Evaluate for Plasmodium parasites.
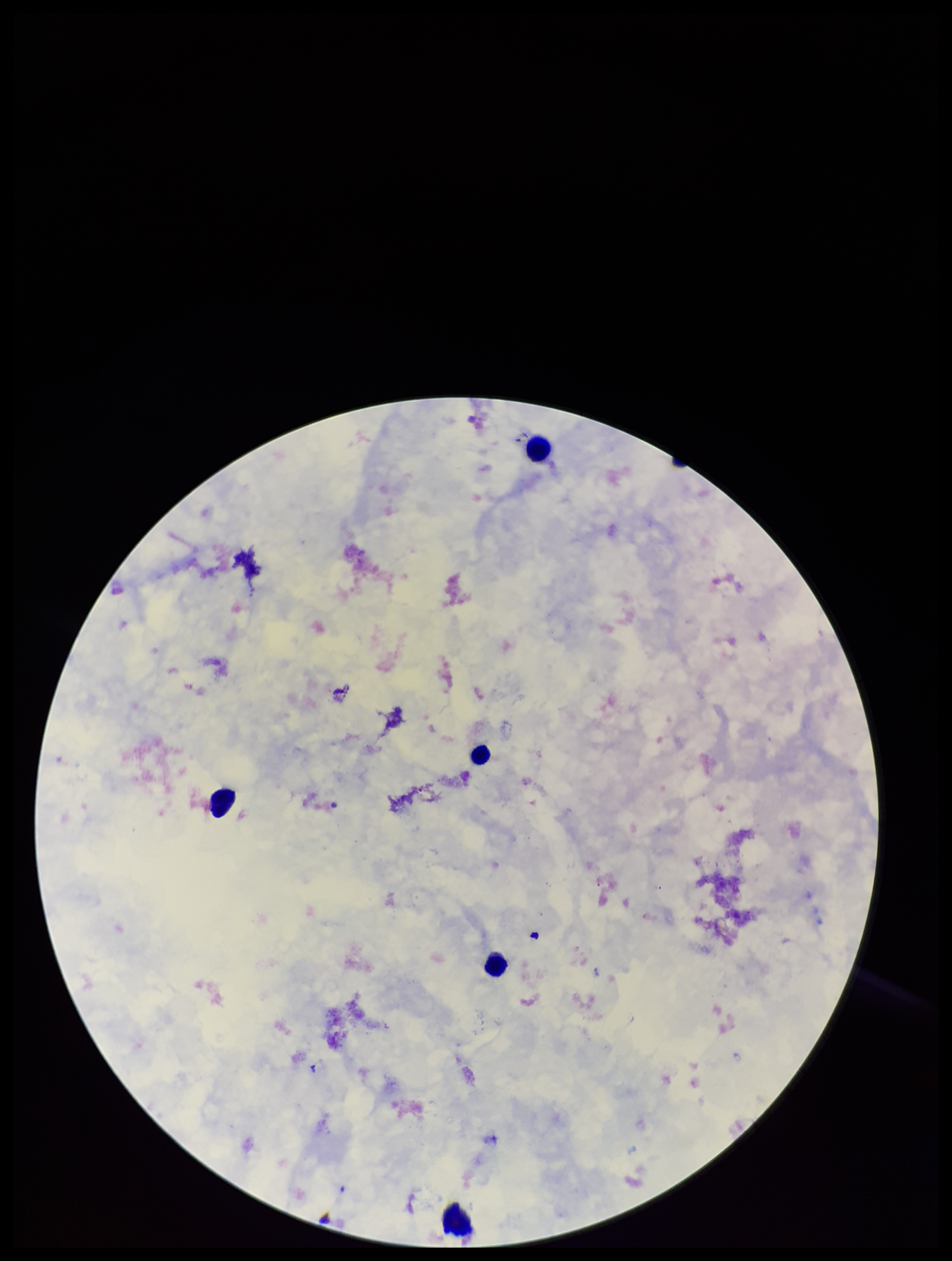

None detected.

Summary:
  - Leukocyte count: 5
  - Stain: Giemsa
  - Preparation: thick
  - Patient malaria status: negative
  - Parasite count: 0
  - Field of view: one from this slide
  - Image size: 952×1261 pixels
  - Capture: smartphone photograph through the microscope eyepiece